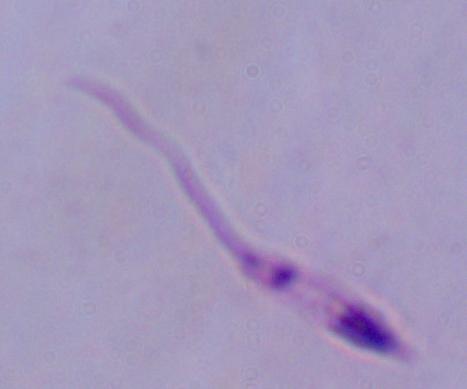

1000x magnification. A Leishmania parasite is shown. Micrograph.